Name the parasite shown.
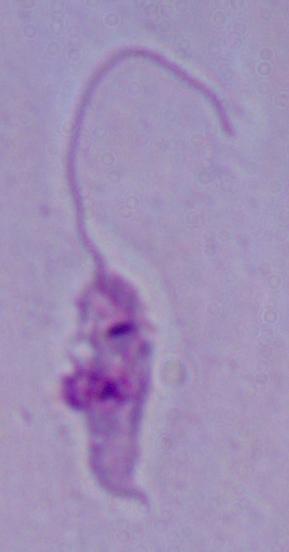
This is Leishmania.

Captured at 1000x magnification. Photomicrograph.